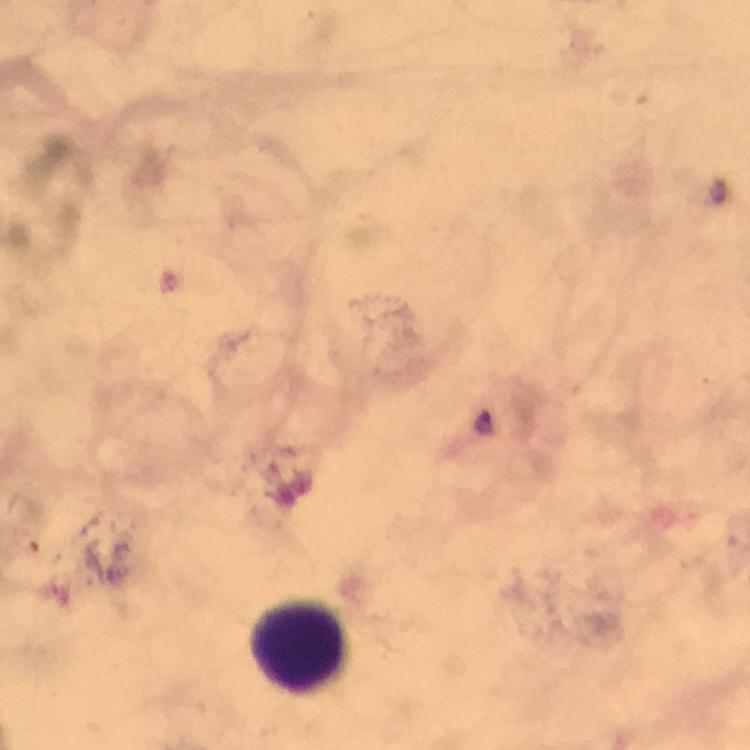

Approximate centers as [x, y] in pixels.
Summary:
  - Leukocyte locations: [302, 644]
  - Malaria parasite locations: [484, 422]
  - Preparation: thick smear
  - Context: from a diagnostic examination for malaria
  - Capture: smartphone camera through the microscope
  - Immersion oil: used
  - Cropped from: one field of view
  - Image size: 750×750 pixels
  - Magnification: 100x
  - Stain: Giemsa